Report the malaria status of this cell.
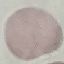
Uninfected.

Summary:
  - Image type: automatically extracted cell patch, resized to 64 × 64 pixels
  - Preparation: thin smear
  - Capture: smartphone through the microscope eyepiece
  - Stain: Giemsa